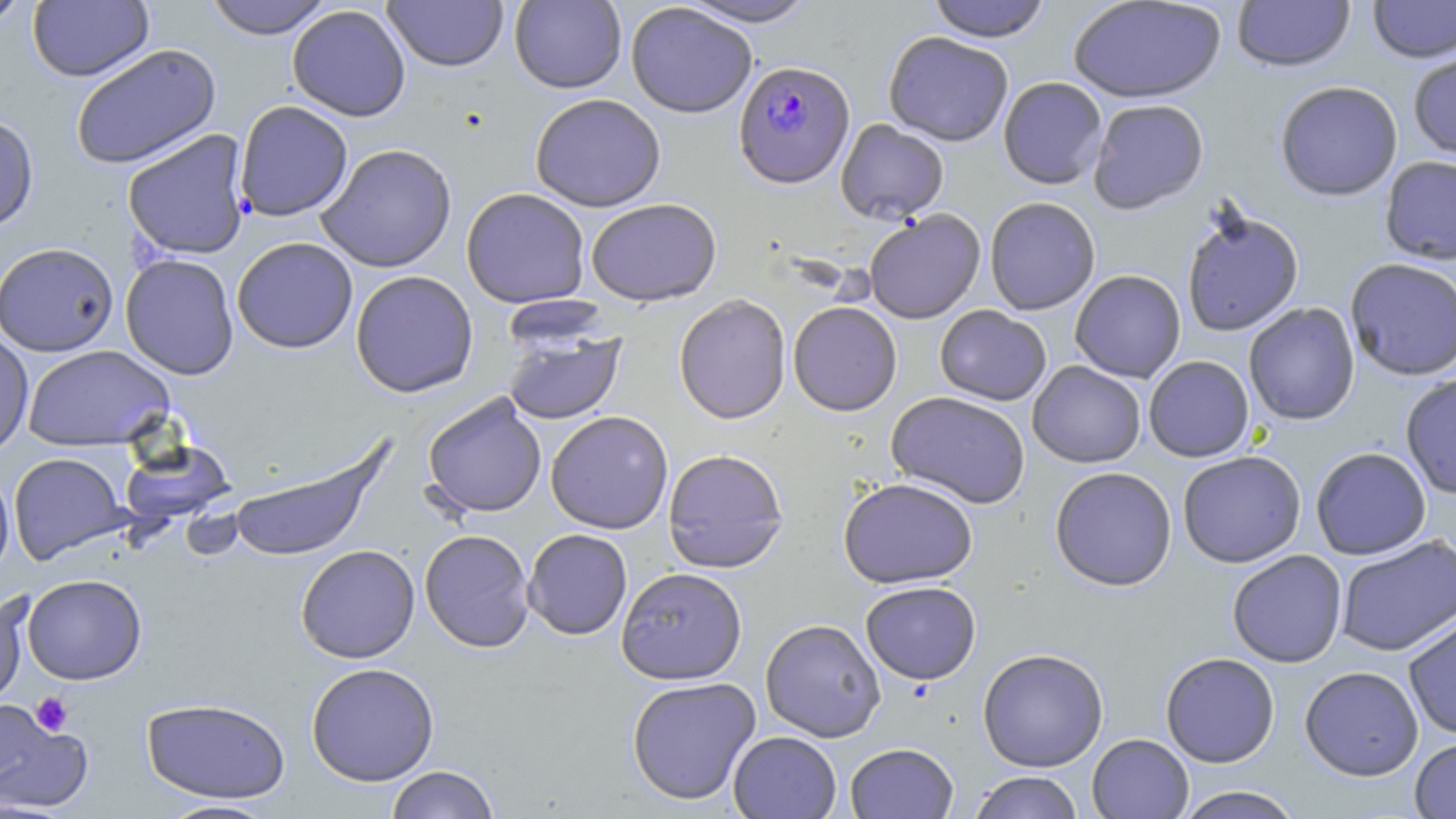

slide_level_diagnosis: Plasmodium falciparum
preparation: thin blood smear
modality: optical microscopy
image_size: 1456×819 pixels
plasmodium_falciparum_infected_red_blood_cell_locations: 'approximate bounding boxes as [x1, y1, x2, y2] in pixels: [734, 59, 855, 188]'
field_of_view: single
uninfected_red_blood_cell_locations: 'approximate bounding boxes as [x1, y1, x2, y2] in pixels: [0, 0, 33, 30], [28, 0, 153, 82], [203, 0, 335, 39], [509, 0, 626, 93], [677, 0, 819, 28], [926, 0, 1052, 43], [1067, 0, 1226, 103], [1232, 0, 1356, 72], [1367, 0, 1456, 63], [382, 1, 509, 72], [626, 2, 758, 118], [287, 5, 411, 121], [883, 31, 1014, 146], [70, 43, 222, 170], [1408, 48, 1456, 160], [998, 76, 1107, 189], [1274, 81, 1403, 201], [529, 93, 666, 211], [1087, 99, 1209, 214], [234, 100, 353, 222], [0, 113, 39, 234], [836, 119, 949, 224], [122, 130, 252, 260], [316, 143, 457, 273], [1380, 155, 1456, 265], [461, 187, 591, 308], [985, 197, 1101, 315], [586, 198, 721, 306], [1181, 206, 1304, 337], [864, 209, 986, 324], [231, 237, 358, 354], [0, 241, 119, 357], [120, 253, 239, 380], [1344, 258, 1456, 380], [350, 270, 478, 397], [1069, 270, 1186, 383], [674, 293, 791, 425], [788, 301, 902, 415], [1244, 303, 1360, 425], [935, 305, 1051, 405], [0, 328, 34, 460], [503, 330, 626, 424], [21, 345, 175, 451], [1144, 355, 1255, 462], [1028, 361, 1146, 467], [1400, 374, 1456, 500], [886, 391, 1031, 509], [422, 393, 547, 518], [545, 410, 673, 534], [120, 440, 236, 525], [227, 443, 388, 563], [1310, 447, 1431, 559], [662, 448, 788, 573], [1177, 451, 1306, 567], [8, 452, 131, 565], [0, 465, 15, 583], [1049, 466, 1177, 591], [838, 477, 978, 588], [522, 528, 632, 640], [419, 529, 535, 652], [1336, 536, 1455, 656], [295, 544, 420, 663], [1227, 550, 1347, 667], [616, 566, 747, 685], [22, 574, 147, 685], [860, 580, 981, 684], [0, 592, 30, 711], [1403, 614, 1456, 740], [760, 619, 886, 741], [977, 648, 1109, 772], [1160, 652, 1280, 768], [306, 662, 440, 786], [1299, 666, 1423, 781], [626, 676, 761, 805], [141, 697, 290, 803], [0, 699, 93, 815], [728, 731, 841, 818], [1087, 733, 1194, 819], [1409, 736, 1456, 818], [845, 742, 958, 818], [384, 765, 500, 819], [968, 771, 1084, 818], [1173, 785, 1305, 819], [156, 799, 281, 818]'
platelet_locations: 'approximate bounding boxes as [x1, y1, x2, y2] in pixels: [30, 692, 73, 736]'
magnification: 1000x
stain: May-Grünwald-Giemsa